Locate every blood parasite and identify its species.
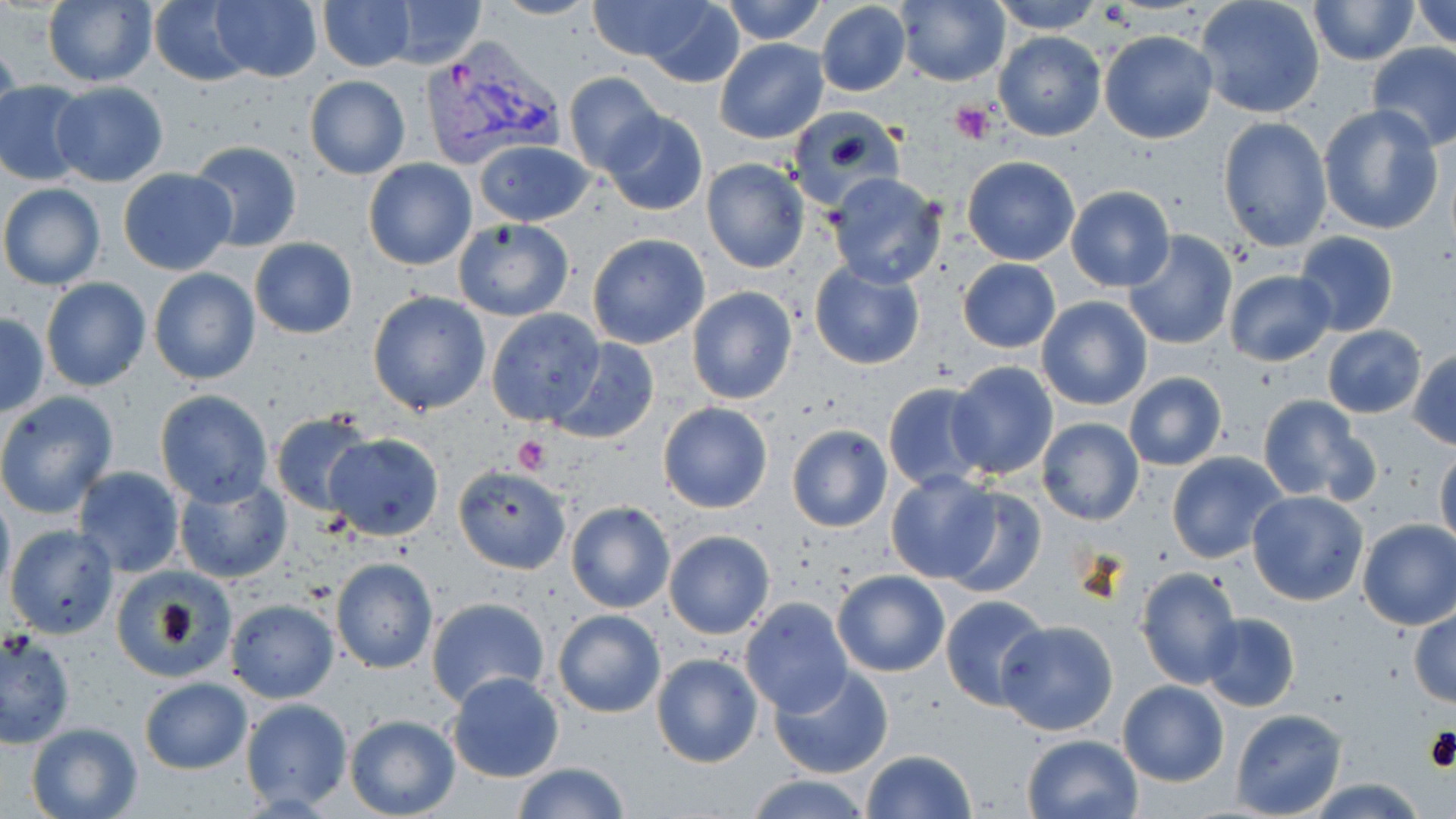

Approximate bounding boxes as [x1, y1, x2, y2] in pixels.
Plasmodium vivax-infected red blood cells: [421, 41, 561, 171].
No Plasmodium falciparum, Plasmodium ovale, Plasmodium malariae, Babesia divergens, or Trypanosoma brucei observed.

Summary:
  - Uninfected red blood cell locations: [42, 0, 159, 89], [149, 0, 252, 86], [316, 0, 416, 71], [381, 0, 487, 69], [488, 0, 597, 20], [586, 0, 719, 62], [716, 0, 830, 45], [897, 0, 1011, 87], [988, 0, 1106, 33], [1195, 0, 1326, 120], [1306, 0, 1417, 66], [1410, 0, 1456, 49], [210, 1, 323, 82], [816, 2, 911, 96], [632, 4, 747, 88], [1099, 30, 1218, 145], [994, 32, 1106, 142], [0, 36, 21, 145], [715, 38, 828, 144], [1367, 42, 1456, 151], [564, 72, 666, 176], [304, 75, 411, 179], [0, 81, 89, 186], [48, 82, 170, 187], [1317, 103, 1444, 236], [783, 106, 906, 211], [602, 110, 708, 216], [1217, 116, 1333, 252], [474, 139, 595, 227], [187, 140, 304, 252], [961, 156, 1080, 266], [701, 158, 809, 274], [363, 159, 478, 271], [117, 168, 237, 276], [825, 173, 949, 291], [0, 184, 105, 291], [1065, 186, 1177, 293], [452, 218, 575, 322], [1122, 229, 1237, 350], [1293, 231, 1400, 336], [586, 233, 709, 349], [249, 238, 358, 339], [956, 257, 1063, 353], [809, 261, 926, 369], [148, 267, 261, 386], [1222, 269, 1337, 366], [40, 278, 151, 392], [686, 286, 798, 404], [368, 291, 491, 414], [1036, 295, 1153, 411], [485, 308, 605, 427], [0, 313, 48, 415], [1320, 327, 1427, 418], [547, 338, 661, 444], [1409, 347, 1456, 450], [945, 361, 1061, 479], [1123, 372, 1227, 471], [882, 381, 993, 492], [0, 391, 119, 519], [155, 391, 274, 507], [1258, 396, 1375, 505], [657, 402, 773, 514], [270, 412, 375, 517], [1037, 418, 1144, 526], [786, 424, 893, 532], [324, 432, 444, 540], [1435, 445, 1456, 549], [1168, 452, 1289, 563], [454, 464, 574, 575], [73, 465, 186, 576], [884, 472, 1002, 585], [173, 476, 291, 585], [0, 488, 14, 595], [868, 489, 985, 644], [942, 489, 1047, 598], [1245, 492, 1369, 607], [564, 501, 674, 612], [1356, 519, 1456, 631], [6, 525, 119, 640], [664, 529, 775, 639], [331, 558, 439, 673], [1135, 565, 1243, 690], [110, 567, 237, 681], [832, 569, 950, 677], [941, 595, 1051, 710], [425, 597, 550, 712], [740, 598, 852, 716], [226, 599, 339, 703], [1409, 606, 1456, 707], [552, 609, 666, 718], [1200, 613, 1300, 711], [997, 620, 1118, 736], [1, 629, 75, 748], [651, 654, 763, 768], [653, 657, 889, 769], [768, 665, 895, 782], [445, 672, 565, 783], [139, 676, 252, 775], [1117, 680, 1229, 786], [239, 698, 354, 813], [1230, 709, 1347, 819], [345, 714, 461, 819], [25, 722, 144, 819], [1021, 733, 1142, 819], [861, 749, 978, 819], [510, 762, 632, 818], [746, 774, 873, 818], [1304, 779, 1431, 817]
  - Platelet locations: [949, 103, 996, 145], [513, 435, 549, 475], [1422, 724, 1454, 775]
  - Slide-level diagnosis: Plasmodium vivax
  - Magnification: 1000x
  - Modality: light microscopy
  - Preparation: thin blood film
  - Stain: May-Grünwald-Giemsa
  - Field of view: one of a larger specimen
  - Image size: 1456×819 pixels